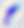

modality = photomicrograph
magnification = 400x
identification = Toxoplasma gondii